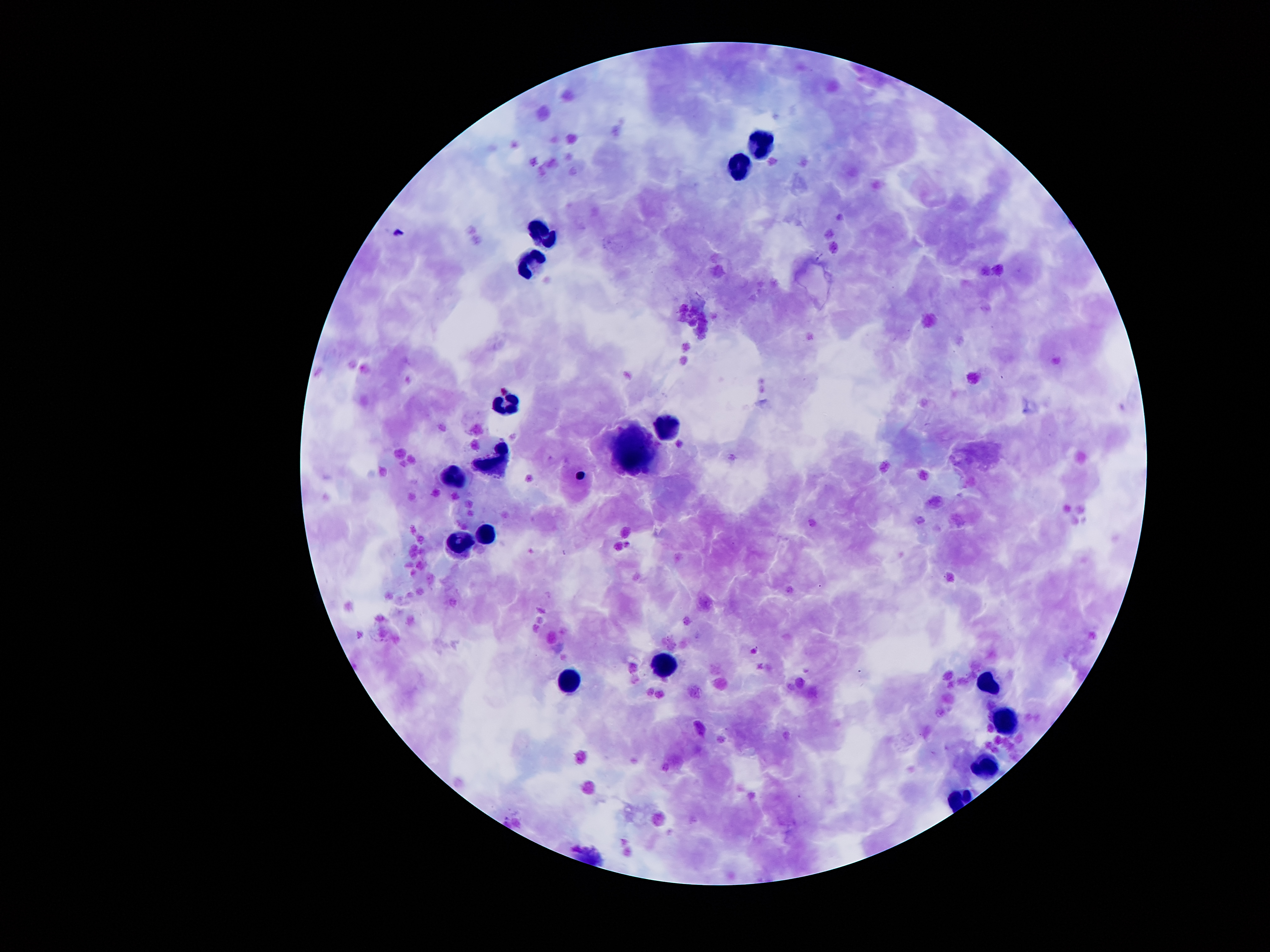
{
  "magnification": "100x",
  "leukocyte_locations": "approximate centers as [x, y] in pixels: [759, 141], [739, 170], [545, 230], [529, 262], [504, 400], [666, 424], [636, 448], [498, 459], [453, 477], [489, 529], [462, 542], [661, 671], [568, 679], [987, 682], [1003, 725], [987, 766]",
  "preparation": "thick blood smear",
  "patient_malaria_status": "infected with Plasmodium falciparum",
  "malaria_parasite_locations": "approximate centers as [x, y] in pixels: [580, 475]",
  "field_of_view": "single",
  "capture": "smartphone camera through the microscope eyepiece",
  "stain": "Giemsa",
  "image_size": "1270×952 pixels"
}